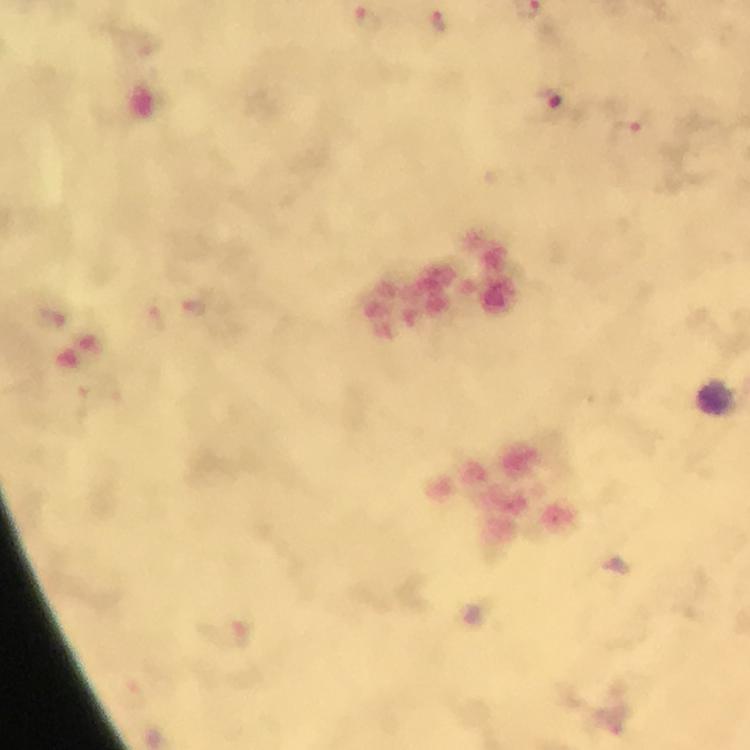

magnification = 100x
immersion oil = used
cropped from = a single field of view
image size = 750×750 pixels
capture = smartphone mounted on the microscope
malaria parasite locations = approximate centers as (x, y) in pixels: (368, 19), (438, 22), (553, 102), (624, 132)
context = from a diagnostic examination for malaria
stain = Giemsa
preparation = thick blood film
leukocyte locations = approximate centers as (x, y) in pixels: (718, 397)